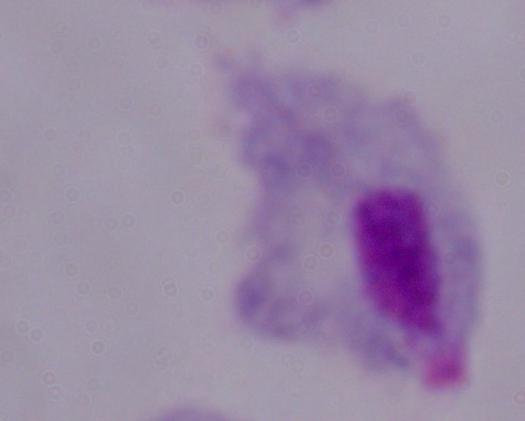
modality = micrograph
magnification = 1000x
identification = trichomonad